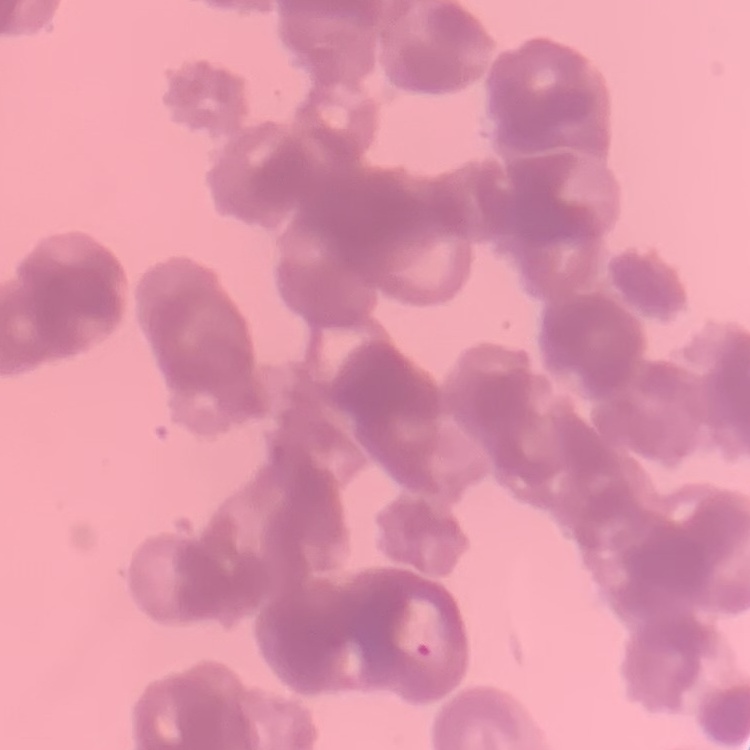

Summary:
  - Erythrocyte morphology: rouleaux formation
  - Preparation: thin blood film
  - Stain: Field's or Giemsa
  - Image type: one tile cut from a larger photomicrograph